State the preparation type.
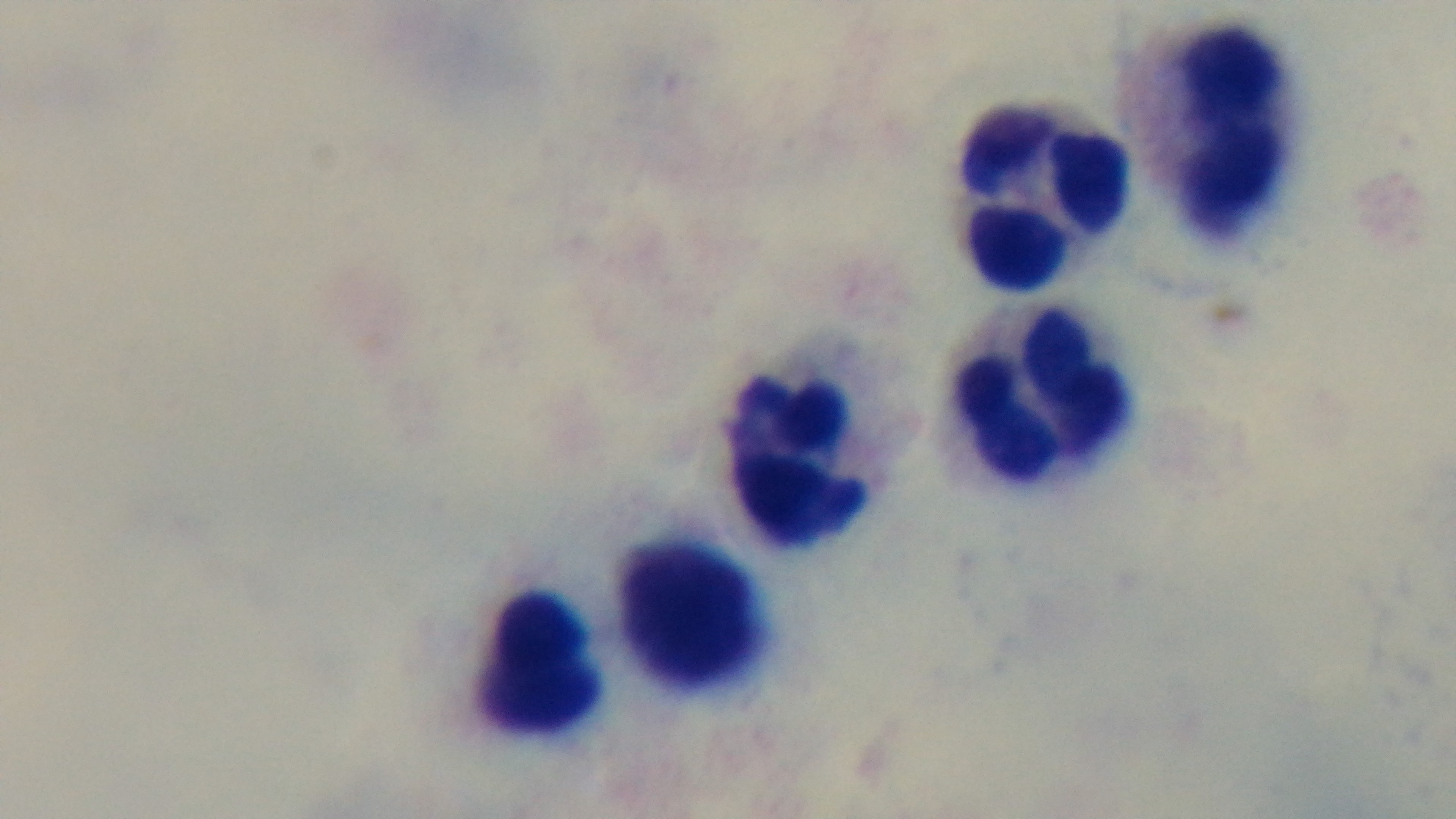
It is a thick blood film.

capture = mounted 4K digital camera
stain = Giemsa
malaria status = uninfected
field of view = single
objective = 100x oil immersion
modality = light microscopy